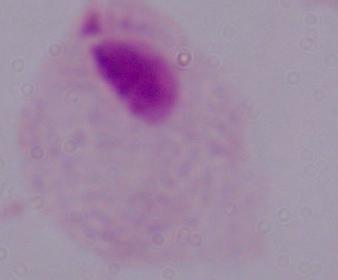

identification = trichomonad
modality = photomicrograph
magnification = 1000x